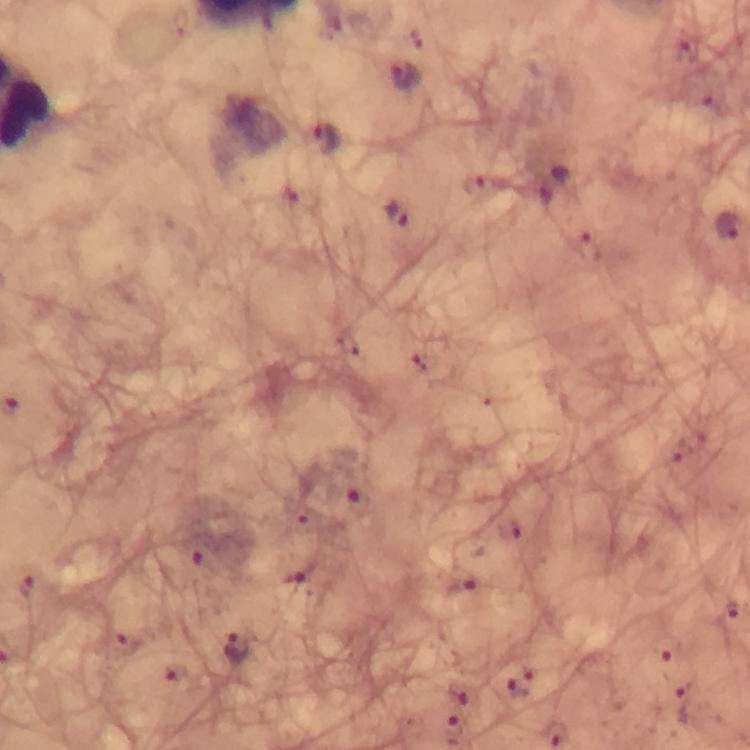
Approximate centers as [x, y] in pixels. Malaria parasite locations: [686, 48], [405, 77], [327, 138], [472, 183], [394, 215], [728, 225], [360, 502], [506, 528], [197, 561], [293, 581], [464, 587], [728, 613], [121, 642], [237, 645], [662, 649], [173, 674], [519, 683], [457, 694], [688, 704], [454, 730]. A crop from one field of view. Image is 750×750 pixels. At 100x magnification. Thick smear. Photographed with a smartphone mounted on the microscope. Giemsa stain. From a diagnostic examination for malaria. Immersion oil applied.